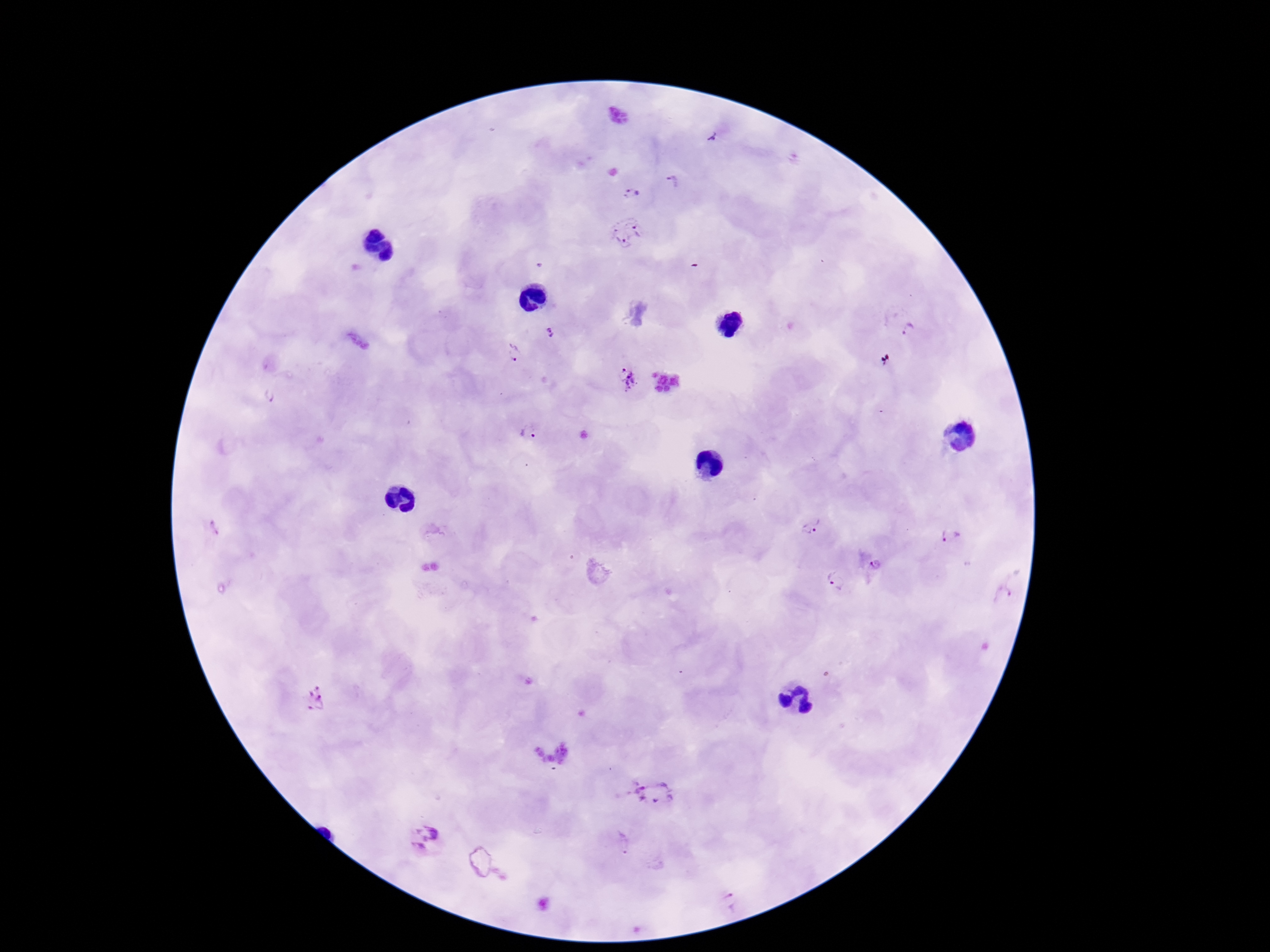

Approximate centers as {x, y} in pixels.
Summary:
  - Plasmodium parasite locations: {712, 136}, {671, 184}, {633, 192}, {626, 231}, {909, 330}, {551, 333}, {513, 353}, {629, 380}, {269, 397}, {528, 430}, {811, 526}, {215, 529}, {951, 538}, {876, 566}, {836, 580}, {1004, 594}, {315, 699}, {653, 792}, {425, 839}, {623, 843}, {729, 900}
  - Field of view: single
  - Patient malaria status: infected
  - Stain: Giemsa
  - Magnification: 100x
  - Capture: smartphone camera through the microscope eyepiece
  - Preparation: thick blood film
  - Image size: 1270×952 pixels